Locate every Plasmodium parasite.
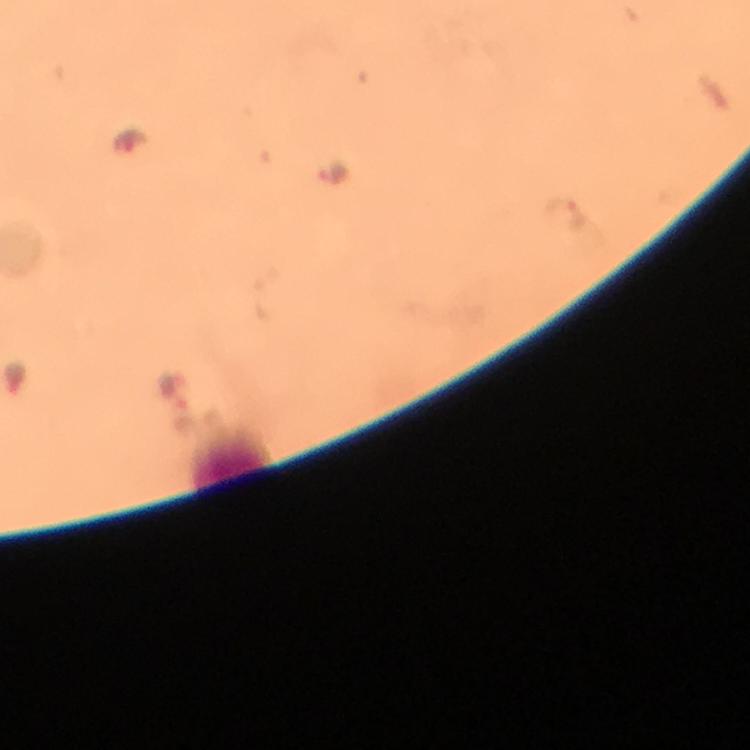
Approximate centers as [x, y] in pixels.
Plasmodium parasites: [132, 145], [329, 172], [575, 214], [15, 378], [170, 384], [183, 415].

Thick blood film. A crop from one field of view. From a diagnostic examination for malaria. Image is 750×750 pixels. At 100x magnification. Immersion oil was used. Giemsa-stained preparation. Photographed through the microscope with a smartphone camera.